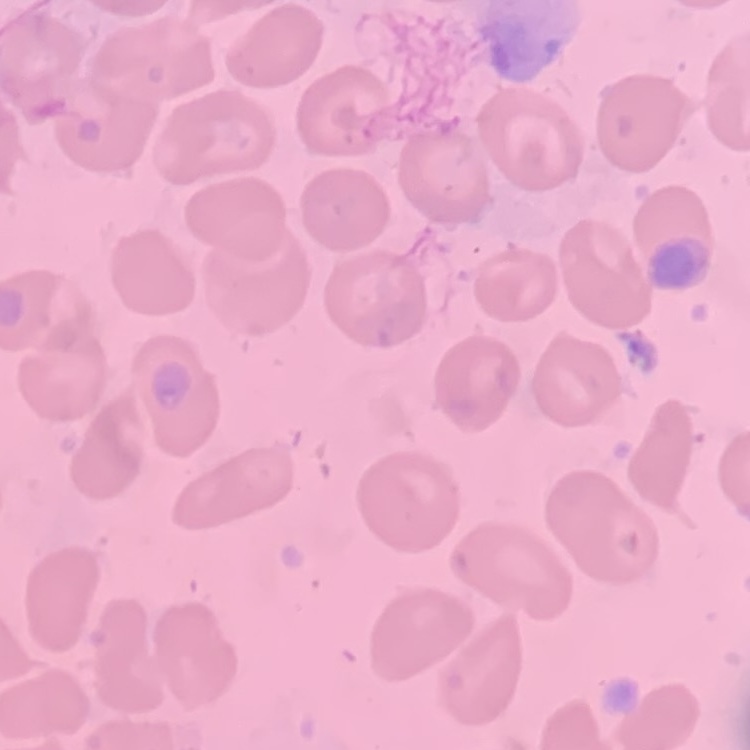

red_blood_cell_morphology: no rouleaux formation
preparation: thin peripheral smear
stain: Field's or Giemsa
image_type: square crop of a larger photomicrograph